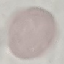 Malaria status: uninfected. Acquired by smartphone through the microscope eyepiece. Giemsa stain. Thin blood film. Cell patch, automatically extracted from a larger field of view and resized to 64 × 64 pixels.